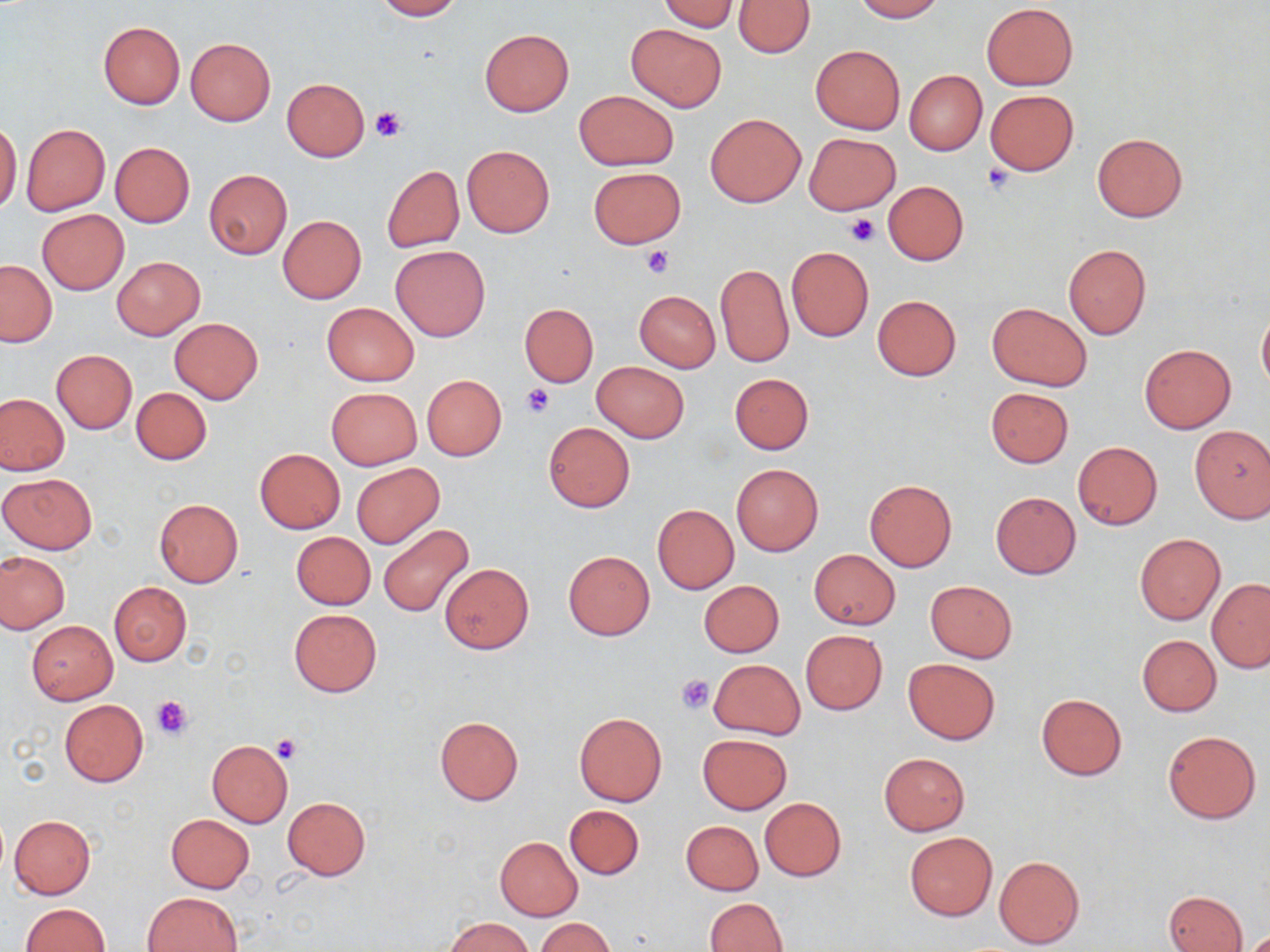

Summary:
  - Coordinate format: approximate bounding boxes as (x1, y1, x2, y2) in pixels
  - Platelet locations: (371, 106, 405, 142), (983, 161, 1014, 192), (844, 215, 878, 246), (640, 247, 674, 278), (521, 381, 555, 417), (676, 674, 714, 714), (151, 695, 192, 739), (271, 734, 303, 764)
  - Uninfected red blood cell locations: (373, 0, 462, 20), (659, 0, 740, 32), (735, 0, 814, 57), (851, 0, 943, 21), (982, 3, 1078, 90), (99, 21, 185, 108), (625, 22, 727, 112), (479, 28, 574, 117), (185, 37, 275, 125), (810, 45, 905, 134), (904, 70, 987, 156), (281, 78, 370, 161), (574, 89, 679, 171), (985, 89, 1079, 175), (706, 113, 806, 207), (0, 122, 21, 214), (22, 123, 110, 215), (1092, 132, 1186, 221), (805, 134, 900, 215), (109, 141, 196, 228), (462, 145, 555, 237), (382, 165, 464, 252), (588, 167, 685, 248), (204, 169, 292, 259), (883, 181, 968, 265), (38, 210, 128, 294), (278, 215, 366, 304), (391, 244, 491, 342), (1062, 244, 1152, 339), (786, 246, 873, 342), (113, 256, 204, 339), (1, 260, 56, 347), (716, 263, 793, 367), (635, 290, 721, 372), (872, 295, 961, 381), (322, 302, 419, 386), (519, 303, 599, 386), (987, 303, 1092, 391), (1258, 308, 1270, 393), (169, 317, 263, 403), (1140, 343, 1235, 433), (52, 349, 137, 433), (591, 361, 689, 443), (730, 373, 814, 454), (422, 375, 507, 460), (131, 387, 212, 465), (327, 387, 422, 469), (985, 387, 1074, 467), (0, 393, 68, 475), (543, 421, 635, 512), (1189, 426, 1270, 523), (1072, 440, 1162, 531), (255, 448, 346, 533), (352, 463, 445, 548), (732, 463, 823, 555), (0, 473, 96, 554), (864, 478, 957, 572), (991, 492, 1081, 579), (154, 499, 243, 587), (652, 503, 739, 595), (378, 525, 474, 616), (291, 531, 375, 609), (1134, 533, 1225, 624), (562, 550, 654, 640), (809, 550, 900, 629), (1, 551, 70, 633), (440, 562, 534, 653), (1207, 579, 1270, 671), (699, 580, 784, 657), (926, 580, 1017, 662), (109, 581, 190, 666), (289, 608, 381, 697), (27, 621, 117, 705), (800, 629, 888, 714), (1137, 634, 1221, 716), (903, 658, 999, 745), (710, 659, 805, 738), (1036, 693, 1127, 779), (58, 699, 149, 787), (574, 713, 667, 807), (435, 716, 523, 804), (1163, 730, 1261, 823), (698, 734, 792, 814), (207, 739, 293, 827), (879, 753, 969, 835), (282, 797, 371, 879), (759, 797, 847, 881), (565, 805, 643, 880), (166, 814, 255, 893), (10, 815, 96, 899), (681, 820, 763, 895), (905, 832, 997, 920), (495, 836, 583, 921), (994, 855, 1085, 949), (143, 891, 242, 952), (1163, 891, 1248, 952), (704, 898, 787, 951), (19, 903, 110, 952), (444, 917, 533, 951), (535, 918, 615, 952)
  - Slide-level diagnosis: negative for blood parasites
  - Stain: May-Grünwald-Giemsa
  - Modality: optical microscopy
  - Field of view: single
  - Image size: 1270×952 pixels
  - Preparation: thin blood smear
  - Magnification: 1000x